Name the blood parasite species.
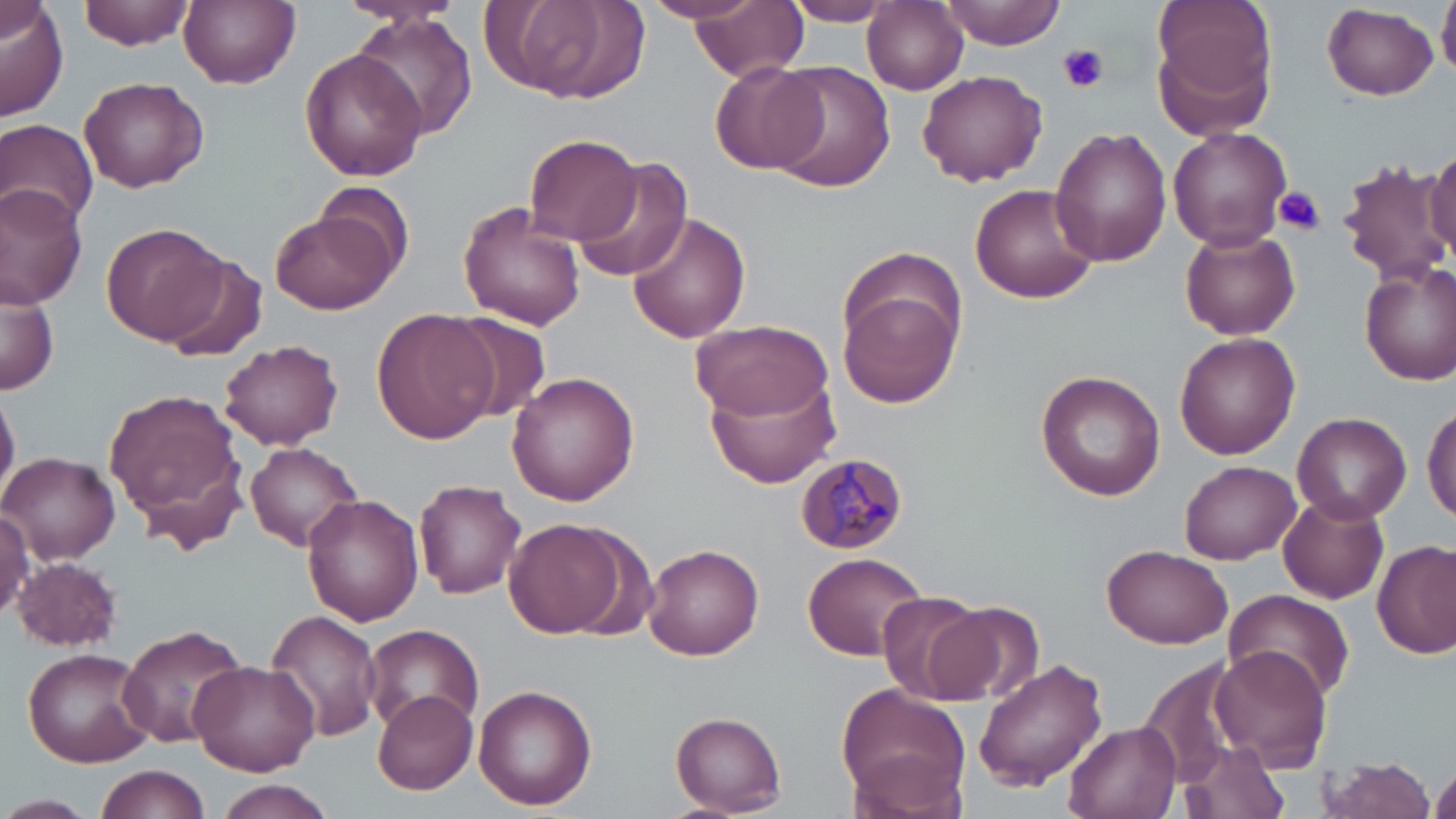
Plasmodium malariae.

Summary:
  - Coordinate format: approximate bounding boxes as (x1,y1)-(x2,y2) corner pairs in pixels
  - Uninfected red blood cell locations: (81,0)-(195,49), (685,0)-(809,82), (779,0)-(901,24), (938,0)-(1064,50), (1149,0)-(1278,131), (1438,0)-(1456,78), (179,1)-(300,89), (863,1)-(968,94), (0,2)-(68,121), (482,2)-(646,109), (1323,5)-(1440,99), (348,11)-(481,144), (300,49)-(426,181), (713,60)-(829,173), (764,61)-(896,192), (917,69)-(1048,186), (78,75)-(208,192), (0,97)-(187,214), (0,116)-(100,231), (1168,125)-(1292,250), (1050,127)-(1172,266), (525,134)-(639,248), (1426,144)-(1456,258), (574,159)-(695,284), (1340,160)-(1448,288), (969,183)-(1099,304), (0,184)-(88,306), (455,201)-(586,329), (269,205)-(401,315), (626,210)-(751,343), (101,223)-(229,345), (1180,227)-(1300,340), (155,255)-(270,362), (1359,263)-(1456,386), (0,273)-(59,397), (841,285)-(963,408), (372,308)-(498,446), (446,313)-(552,423), (688,318)-(834,420), (1175,333)-(1300,459), (220,338)-(344,450), (1036,368)-(1168,501), (507,371)-(643,506), (706,371)-(843,489), (0,384)-(20,510), (104,387)-(250,544), (1422,402)-(1456,524), (1293,411)-(1409,523), (243,442)-(364,552), (2,451)-(120,563), (1180,460)-(1299,564), (415,478)-(528,598), (300,493)-(423,625), (1278,495)-(1389,603), (0,509)-(34,620), (503,518)-(629,638), (1374,539)-(1456,659), (642,543)-(765,660), (1102,545)-(1233,649), (803,551)-(928,660), (13,557)-(125,651), (1224,589)-(1355,701), (873,592)-(997,703), (930,602)-(1045,709), (264,610)-(384,742), (115,622)-(250,749), (361,622)-(485,731), (1207,645)-(1332,771), (20,647)-(155,768), (1138,655)-(1252,790), (188,659)-(320,774), (972,659)-(1108,792), (835,683)-(971,817), (474,684)-(596,810), (372,689)-(480,796), (670,711)-(785,816), (1065,719)-(1181,819), (1174,739)-(1293,819), (1313,754)-(1440,819), (1429,756)-(1456,819), (95,765)-(212,819), (209,779)-(338,819), (0,794)-(97,819)
  - Plasmodium malariae-infected red blood cell locations: (793,452)-(909,553)
  - Platelet locations: (1058,43)-(1109,93), (1274,186)-(1325,235)
  - Preparation: thin blood film
  - Magnification: 1000x
  - Stain: May-Grünwald-Giemsa
  - Field of view: one of a larger specimen
  - Image size: 1456×819 pixels
  - Modality: optical microscopy